Outline each Plasmodium vivax-infected red blood cell.
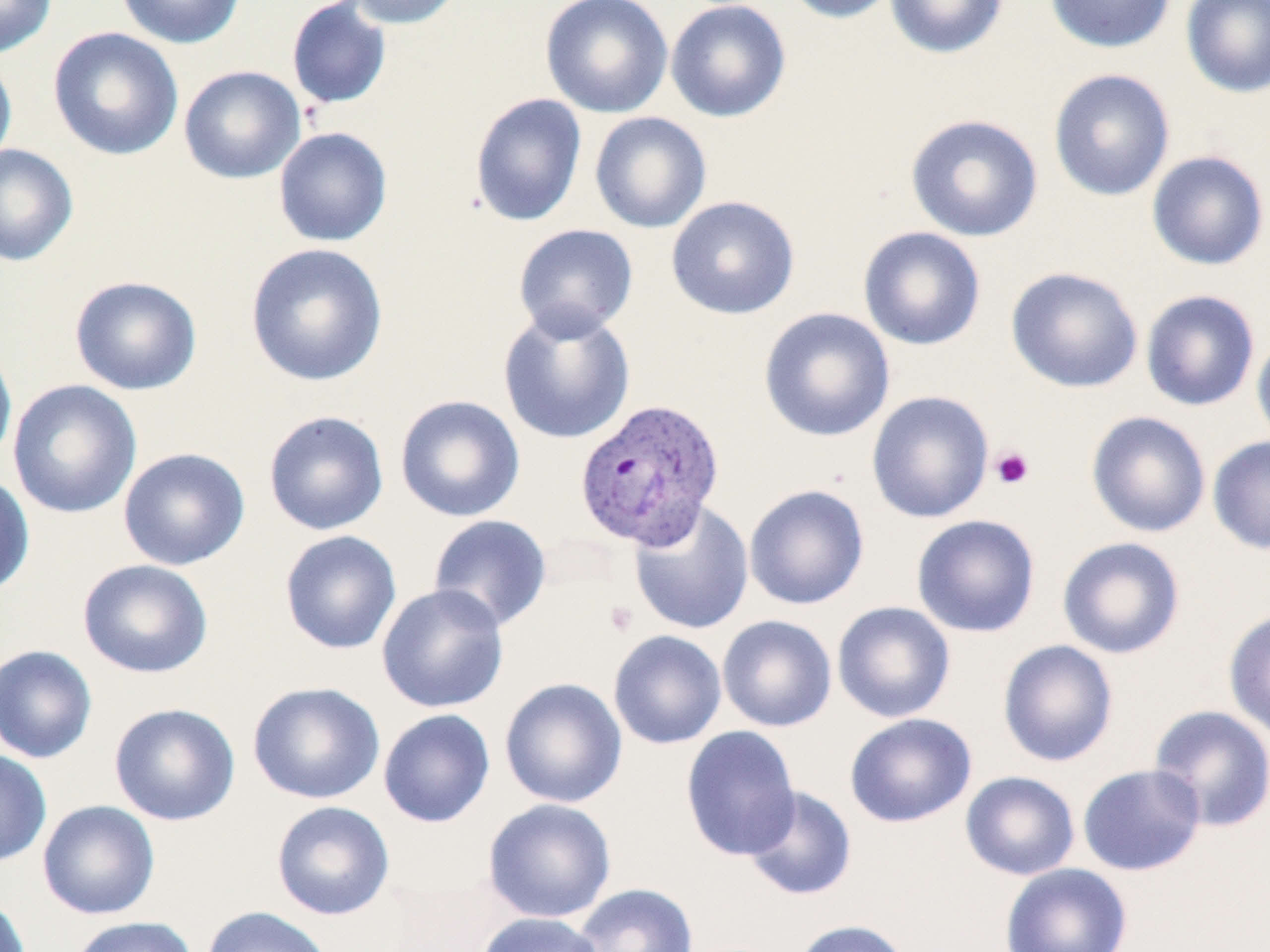
Approximate bounding boxes as named x1/y1/x2/y2 corners in pixels.
Plasmodium vivax-infected red blood cells: (x1=573, y1=396, x2=725, y2=552).

slide-level diagnosis = Plasmodium vivax
field of view = single
uninfected red blood cell locations = approximate bounding boxes as named x1/y1/x2/y2 corners in pixels: (x1=0, y1=0, x2=57, y2=58), (x1=116, y1=0, x2=246, y2=49), (x1=343, y1=0, x2=466, y2=29), (x1=540, y1=0, x2=673, y2=118), (x1=665, y1=0, x2=792, y2=123), (x1=778, y1=0, x2=901, y2=23), (x1=884, y1=0, x2=1009, y2=59), (x1=1044, y1=0, x2=1176, y2=54), (x1=1180, y1=0, x2=1270, y2=97), (x1=287, y1=1, x2=392, y2=110), (x1=47, y1=26, x2=184, y2=161), (x1=0, y1=53, x2=17, y2=171), (x1=178, y1=65, x2=305, y2=184), (x1=1048, y1=68, x2=1175, y2=202), (x1=469, y1=92, x2=588, y2=227), (x1=589, y1=111, x2=712, y2=234), (x1=905, y1=113, x2=1044, y2=242), (x1=273, y1=127, x2=392, y2=247), (x1=0, y1=144, x2=79, y2=267), (x1=1146, y1=150, x2=1270, y2=271), (x1=666, y1=195, x2=800, y2=320), (x1=513, y1=223, x2=638, y2=340), (x1=858, y1=226, x2=986, y2=350), (x1=244, y1=242, x2=388, y2=387), (x1=1006, y1=266, x2=1143, y2=393), (x1=69, y1=275, x2=202, y2=395), (x1=1140, y1=289, x2=1260, y2=412), (x1=497, y1=305, x2=636, y2=445), (x1=759, y1=307, x2=895, y2=443), (x1=1251, y1=329, x2=1270, y2=452), (x1=0, y1=336, x2=17, y2=471), (x1=7, y1=379, x2=142, y2=519), (x1=866, y1=390, x2=994, y2=523), (x1=394, y1=394, x2=525, y2=523), (x1=263, y1=410, x2=389, y2=536), (x1=1085, y1=410, x2=1211, y2=538), (x1=1207, y1=436, x2=1270, y2=555), (x1=118, y1=447, x2=250, y2=570), (x1=0, y1=472, x2=35, y2=598), (x1=744, y1=483, x2=869, y2=611), (x1=628, y1=500, x2=754, y2=635), (x1=427, y1=514, x2=552, y2=632), (x1=910, y1=514, x2=1041, y2=638), (x1=279, y1=529, x2=402, y2=655), (x1=1057, y1=536, x2=1186, y2=659), (x1=77, y1=558, x2=214, y2=679), (x1=376, y1=583, x2=509, y2=713), (x1=832, y1=600, x2=956, y2=723), (x1=1223, y1=608, x2=1270, y2=740), (x1=717, y1=614, x2=837, y2=732), (x1=608, y1=629, x2=727, y2=750), (x1=997, y1=639, x2=1119, y2=767), (x1=0, y1=644, x2=98, y2=764), (x1=499, y1=677, x2=628, y2=808), (x1=247, y1=681, x2=385, y2=804), (x1=109, y1=702, x2=241, y2=826), (x1=1148, y1=704, x2=1270, y2=832), (x1=378, y1=709, x2=495, y2=828), (x1=844, y1=713, x2=977, y2=828), (x1=680, y1=725, x2=801, y2=861), (x1=0, y1=749, x2=52, y2=867), (x1=1077, y1=763, x2=1206, y2=876), (x1=960, y1=771, x2=1080, y2=880), (x1=742, y1=785, x2=857, y2=901), (x1=483, y1=799, x2=616, y2=923), (x1=37, y1=800, x2=160, y2=920), (x1=271, y1=800, x2=395, y2=920), (x1=999, y1=862, x2=1133, y2=952), (x1=572, y1=882, x2=699, y2=952), (x1=0, y1=892, x2=32, y2=952), (x1=201, y1=906, x2=334, y2=952), (x1=475, y1=912, x2=607, y2=952), (x1=67, y1=915, x2=199, y2=952), (x1=790, y1=919, x2=913, y2=952)
platelet locations = approximate bounding boxes as named x1/y1/x2/y2 corners in pixels: (x1=990, y1=446, x2=1034, y2=489), (x1=605, y1=601, x2=638, y2=636)
stain = May-Grünwald-Giemsa
magnification = 1000x
preparation = thin blood smear
modality = optical microscopy
image size = 1270×952 pixels